Assess this cell for malaria.
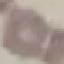

It is uninfected.

stain = Giemsa
image type = automatically extracted cell patch, resized to 64 × 64 pixels
capture = smartphone camera at the microscope eyepiece
preparation = thin blood smear